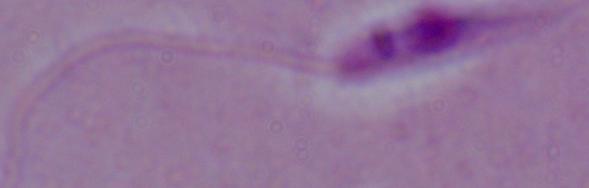

Summary:
  - Magnification: 1000x
  - Modality: photomicrograph
  - Identification: Leishmania